Assess this cell for malaria.
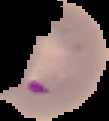

It is parasitized.

Image is 109×121 pixels. From a thin blood smear. Segmented cell region on a black background.